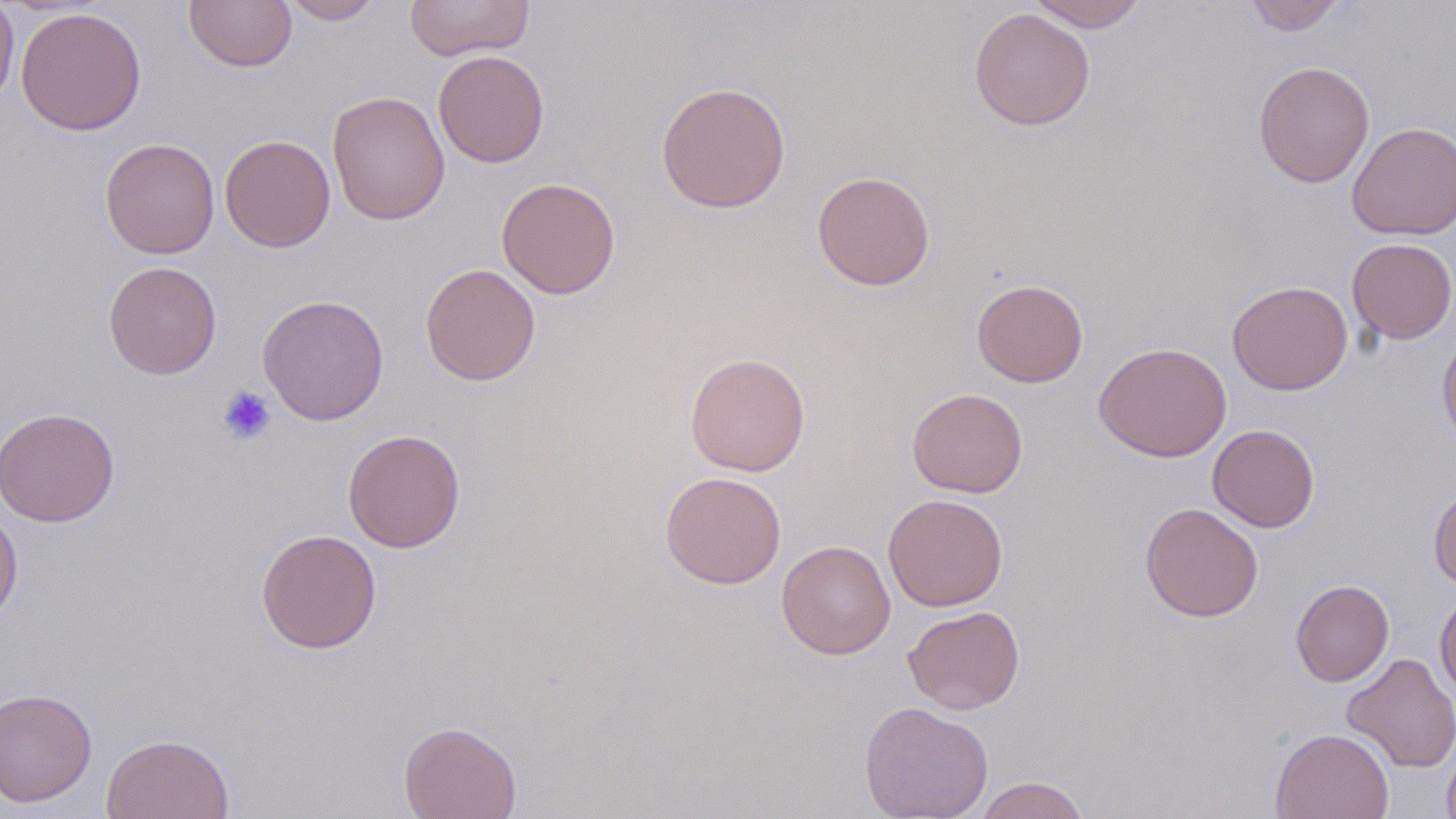
Approximate bounding boxes as named x1/y1/x2/y2 corners in pixels. Platelet locations: (x1=217, y1=385, x2=276, y2=444). Uninfected red blood cell locations: (x1=0, y1=0, x2=19, y2=108), (x1=184, y1=0, x2=297, y2=72), (x1=281, y1=0, x2=385, y2=25), (x1=404, y1=0, x2=535, y2=61), (x1=1026, y1=0, x2=1148, y2=32), (x1=1245, y1=0, x2=1345, y2=35), (x1=15, y1=6, x2=146, y2=136), (x1=969, y1=8, x2=1095, y2=131), (x1=432, y1=49, x2=550, y2=168), (x1=1253, y1=61, x2=1375, y2=188), (x1=655, y1=81, x2=791, y2=214), (x1=327, y1=90, x2=450, y2=226), (x1=1347, y1=121, x2=1455, y2=240), (x1=220, y1=134, x2=335, y2=252), (x1=99, y1=138, x2=220, y2=259), (x1=812, y1=171, x2=935, y2=290), (x1=496, y1=177, x2=620, y2=299), (x1=1346, y1=238, x2=1456, y2=344), (x1=103, y1=261, x2=222, y2=379), (x1=421, y1=263, x2=541, y2=385), (x1=972, y1=279, x2=1088, y2=387), (x1=1227, y1=280, x2=1353, y2=395), (x1=257, y1=294, x2=390, y2=425), (x1=1437, y1=328, x2=1456, y2=449), (x1=1093, y1=341, x2=1232, y2=462), (x1=685, y1=352, x2=811, y2=476), (x1=907, y1=387, x2=1028, y2=498), (x1=0, y1=407, x2=119, y2=527), (x1=1207, y1=424, x2=1320, y2=532), (x1=343, y1=429, x2=466, y2=552), (x1=659, y1=471, x2=786, y2=588), (x1=1428, y1=485, x2=1456, y2=590), (x1=883, y1=493, x2=1008, y2=611), (x1=1139, y1=502, x2=1264, y2=622), (x1=0, y1=503, x2=23, y2=627), (x1=255, y1=528, x2=382, y2=654), (x1=776, y1=540, x2=896, y2=659), (x1=1291, y1=579, x2=1394, y2=687), (x1=1434, y1=589, x2=1456, y2=701), (x1=903, y1=605, x2=1025, y2=714), (x1=1341, y1=652, x2=1456, y2=773), (x1=0, y1=687, x2=97, y2=808), (x1=859, y1=701, x2=994, y2=819), (x1=398, y1=720, x2=522, y2=819), (x1=1271, y1=727, x2=1394, y2=819), (x1=100, y1=732, x2=234, y2=819), (x1=1441, y1=739, x2=1456, y2=819), (x1=973, y1=776, x2=1090, y2=819). Slide-level diagnosis: negative for blood parasites. Image is 1456×819 pixels. One field of a larger specimen. Light microscopy. Captured at 1000x magnification. May-Grünwald-Giemsa stain. Thin blood film.